Assess the morphology of the red blood cells.
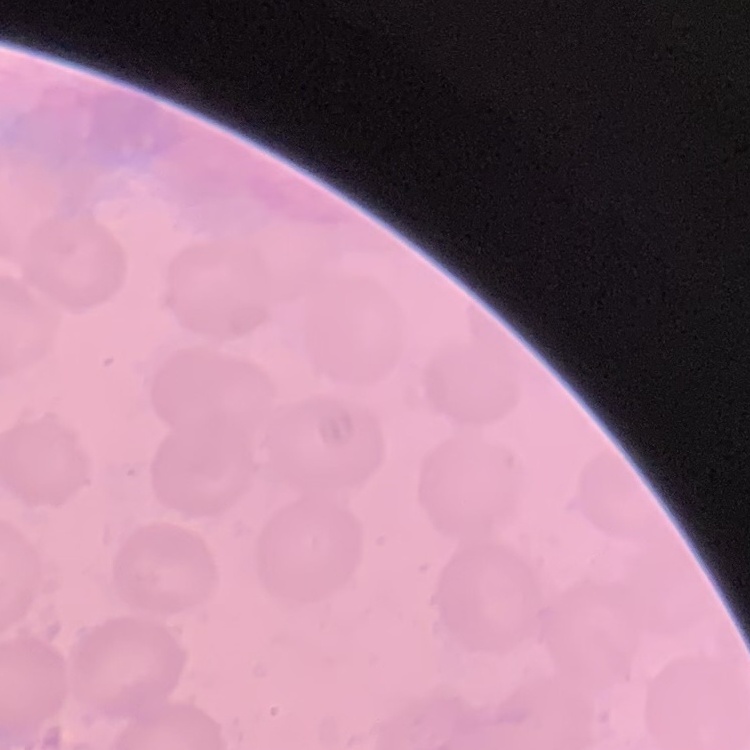
No rouleaux formation.

Thin peripheral smear. One tile cut from a larger photomicrograph. Stained with either Field's or Giemsa.